Assess this cell for malaria.
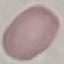

Uninfected.

Giemsa-stained preparation. Cell patch, automatically extracted from a larger field of view and resized to 64 × 64 pixels. Photographed with a smartphone camera at the microscope eyepiece. Thin blood smear.